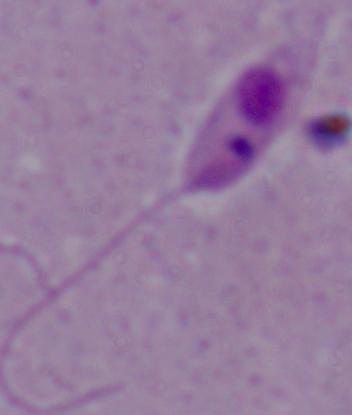

Captured at 1000x magnification. Photomicrograph. A Leishmania parasite is shown.